Give the extent of all Plasmodium falciparum-infected red blood cells.
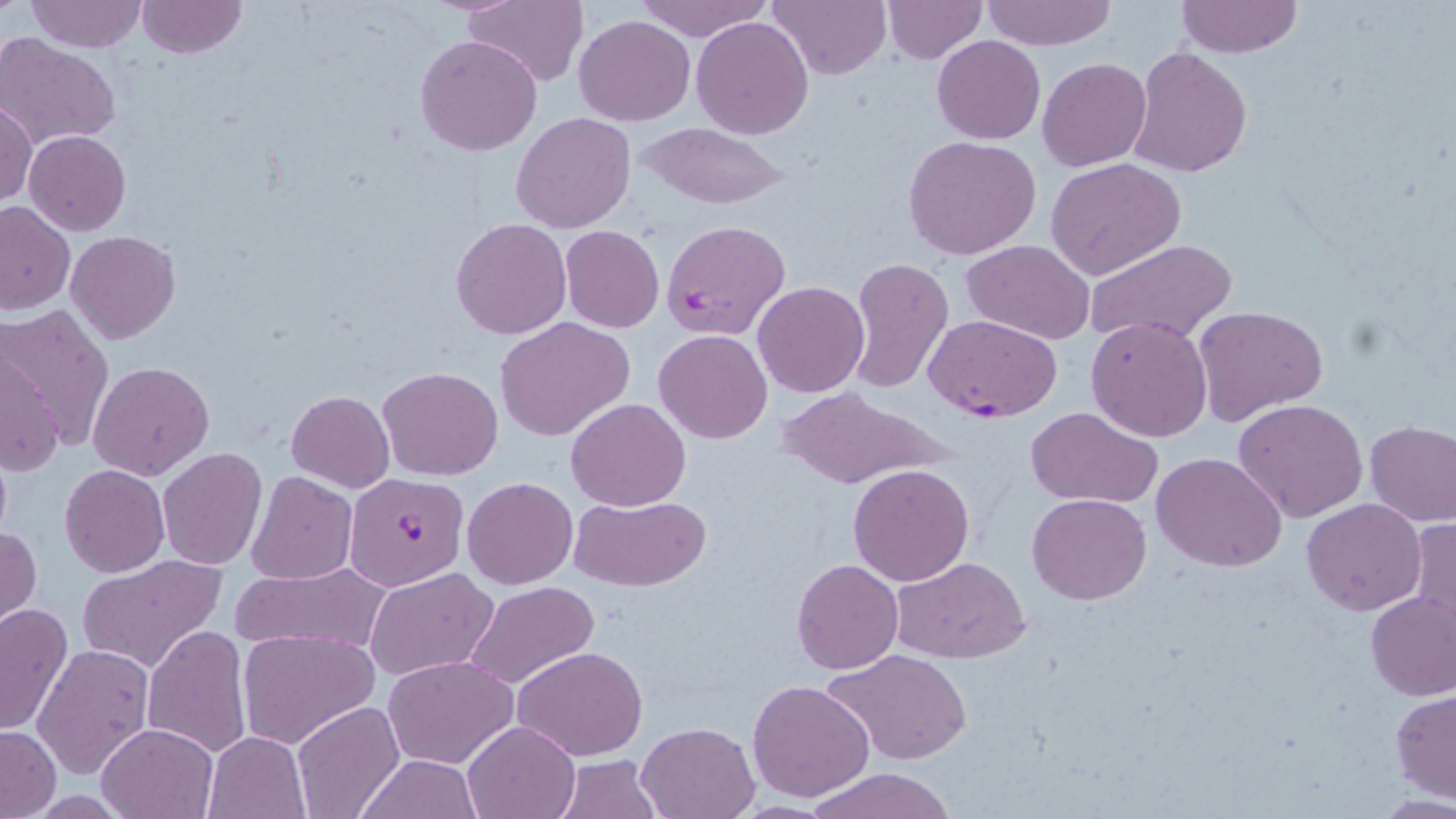

Approximate bounding boxes as named x1/y1/x2/y2 corners in pixels.
Plasmodium falciparum-infected red blood cells: (x1=661, y1=218, x2=792, y2=340), (x1=924, y1=314, x2=1061, y2=422), (x1=345, y1=472, x2=471, y2=590).

slide-level diagnosis = Plasmodium falciparum
modality = light microscopy
stain = May-Grünwald-Giemsa
image size = 1456×819 pixels
uninfected red blood cell locations = approximate bounding boxes as named x1/y1/x2/y2 corners in pixels: (x1=26, y1=0, x2=144, y2=53), (x1=766, y1=0, x2=892, y2=80), (x1=982, y1=0, x2=1115, y2=49), (x1=135, y1=1, x2=247, y2=60), (x1=462, y1=1, x2=588, y2=87), (x1=630, y1=1, x2=773, y2=42), (x1=880, y1=1, x2=987, y2=64), (x1=1176, y1=1, x2=1303, y2=56), (x1=575, y1=14, x2=694, y2=126), (x1=691, y1=16, x2=814, y2=139), (x1=414, y1=34, x2=542, y2=157), (x1=932, y1=34, x2=1045, y2=145), (x1=0, y1=35, x2=122, y2=148), (x1=1129, y1=47, x2=1251, y2=177), (x1=1037, y1=58, x2=1152, y2=171), (x1=1, y1=100, x2=37, y2=207), (x1=512, y1=112, x2=637, y2=232), (x1=637, y1=122, x2=792, y2=210), (x1=24, y1=130, x2=131, y2=236), (x1=903, y1=135, x2=1042, y2=260), (x1=1046, y1=158, x2=1186, y2=279), (x1=0, y1=200, x2=74, y2=315), (x1=450, y1=218, x2=572, y2=339), (x1=560, y1=226, x2=666, y2=333), (x1=66, y1=230, x2=180, y2=343), (x1=1083, y1=239, x2=1235, y2=349), (x1=961, y1=241, x2=1095, y2=344), (x1=845, y1=257, x2=954, y2=394), (x1=752, y1=281, x2=869, y2=399), (x1=1193, y1=304, x2=1329, y2=429), (x1=2, y1=305, x2=114, y2=451), (x1=1086, y1=316, x2=1214, y2=442), (x1=494, y1=317, x2=635, y2=441), (x1=654, y1=330, x2=773, y2=444), (x1=0, y1=348, x2=62, y2=479), (x1=88, y1=360, x2=215, y2=481), (x1=378, y1=366, x2=504, y2=480), (x1=775, y1=389, x2=940, y2=490), (x1=286, y1=391, x2=394, y2=492), (x1=565, y1=397, x2=691, y2=511), (x1=1234, y1=398, x2=1369, y2=522), (x1=1024, y1=406, x2=1165, y2=509), (x1=1365, y1=420, x2=1456, y2=527), (x1=156, y1=449, x2=266, y2=570), (x1=1152, y1=452, x2=1287, y2=572), (x1=848, y1=462, x2=976, y2=586), (x1=59, y1=464, x2=169, y2=578), (x1=248, y1=472, x2=357, y2=585), (x1=461, y1=476, x2=578, y2=589), (x1=571, y1=494, x2=710, y2=591), (x1=1026, y1=494, x2=1150, y2=605), (x1=1303, y1=498, x2=1427, y2=616), (x1=1405, y1=517, x2=1456, y2=644), (x1=1, y1=525, x2=41, y2=640), (x1=76, y1=555, x2=227, y2=673), (x1=890, y1=556, x2=1031, y2=664), (x1=792, y1=558, x2=904, y2=675), (x1=231, y1=562, x2=391, y2=656), (x1=365, y1=567, x2=496, y2=680), (x1=464, y1=581, x2=600, y2=691), (x1=1364, y1=589, x2=1456, y2=701), (x1=0, y1=603, x2=74, y2=737), (x1=141, y1=625, x2=251, y2=760), (x1=237, y1=629, x2=378, y2=749), (x1=33, y1=643, x2=156, y2=781), (x1=512, y1=645, x2=650, y2=761), (x1=825, y1=647, x2=972, y2=766), (x1=384, y1=655, x2=518, y2=768), (x1=747, y1=680, x2=875, y2=803), (x1=1391, y1=690, x2=1456, y2=801), (x1=293, y1=702, x2=405, y2=819), (x1=461, y1=719, x2=581, y2=818), (x1=636, y1=720, x2=761, y2=817), (x1=95, y1=721, x2=220, y2=818), (x1=0, y1=725, x2=60, y2=816), (x1=202, y1=732, x2=309, y2=818), (x1=355, y1=754, x2=483, y2=818), (x1=554, y1=755, x2=660, y2=819), (x1=804, y1=768, x2=957, y2=819)
field of view = single
magnification = 1000x
preparation = thin blood smear